Assess the morphology of the erythrocytes.
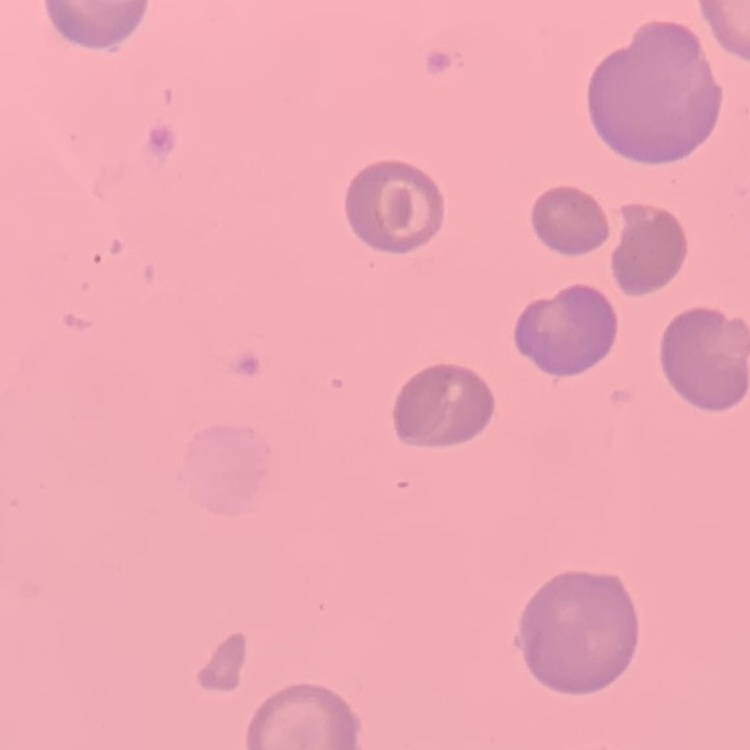

No rouleaux formation.

Thin peripheral smear. Stained with either Field's or Giemsa. Square crop of a larger photomicrograph.